Report the malaria status of this cell.
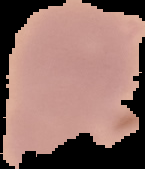
It is uninfected.

Summary:
  - Image size: 145×169 pixels
  - Image type: segmented cell region with the area outside set to black
  - Preparation: thin blood smear